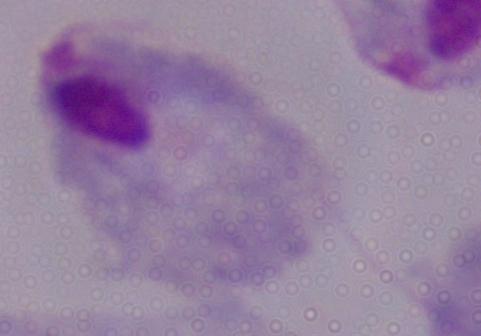 1000x magnification. A trichomonad is seen. Photomicrograph.